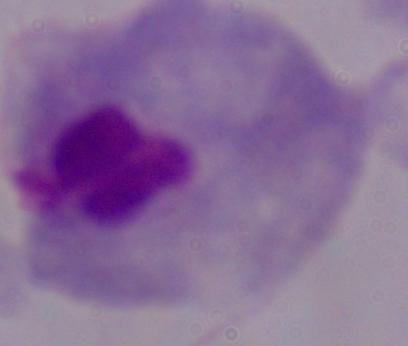
identification = trichomonad
modality = micrograph
magnification = 1000x